Name the blood parasite species.
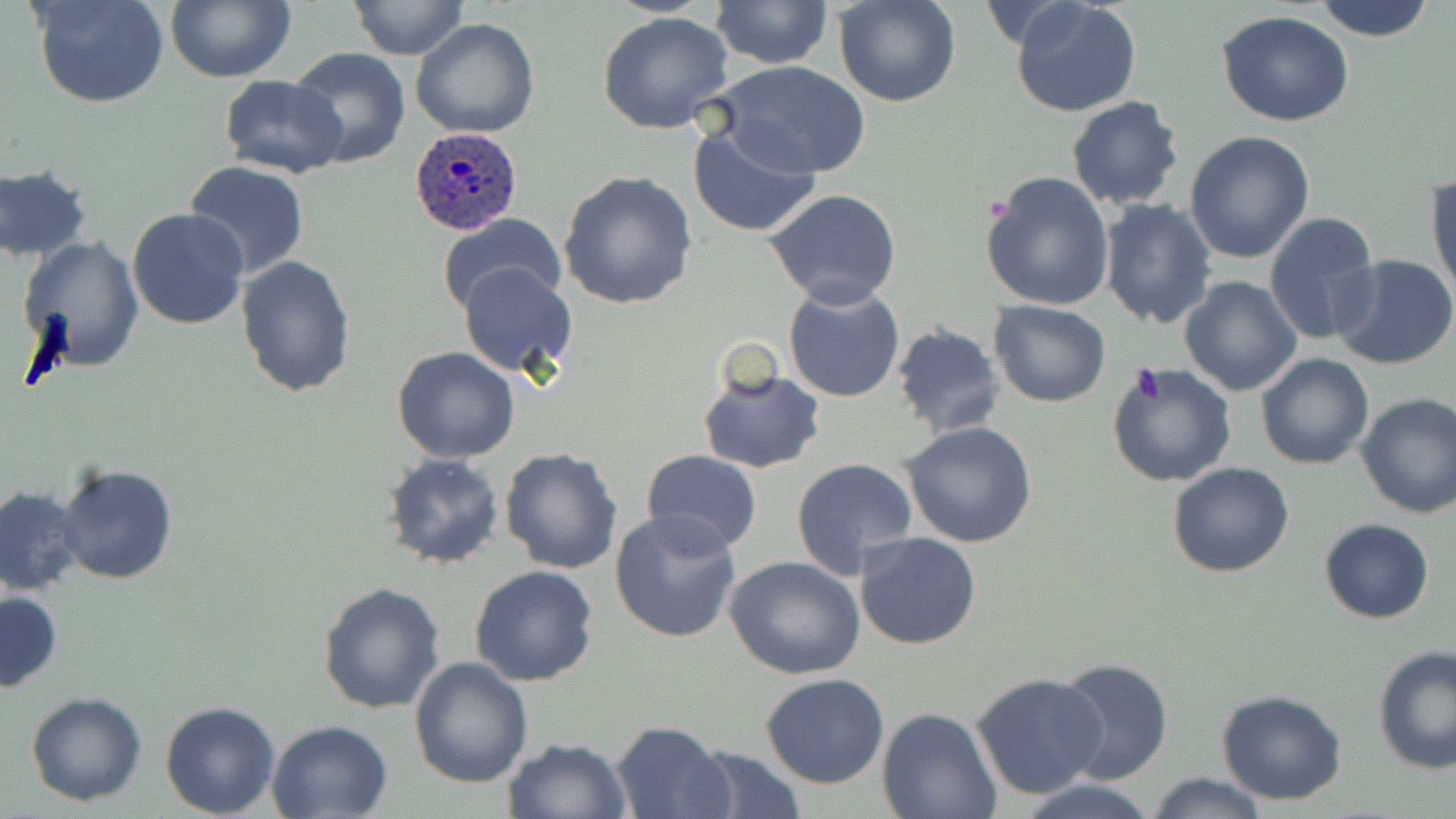
Plasmodium ovale.

stain = May-Grünwald-Giemsa
modality = light microscopy
preparation = thin blood film
image size = 1456×819 pixels
magnification = 1000x
Plasmodium ovale-infected red blood cell locations = approximate bounding boxes as (x1, y1, x2, y2) in pixels: (408, 127, 523, 236)
field of view = one of a larger specimen
platelet locations = approximate bounding boxes as (x1, y1, x2, y2) in pixels: (1127, 362, 1165, 409)
uninfected red blood cell locations = approximate bounding boxes as (x1, y1, x2, y2) in pixels: (30, 0, 169, 108), (166, 0, 294, 83), (349, 0, 469, 62), (711, 0, 833, 70), (834, 0, 961, 107), (1009, 0, 1143, 118), (1311, 0, 1439, 42), (1216, 11, 1357, 128), (597, 12, 735, 135), (410, 18, 541, 138), (287, 48, 413, 170), (711, 60, 872, 180), (217, 73, 346, 178), (1064, 95, 1185, 210), (685, 121, 823, 239), (1185, 131, 1315, 263), (185, 160, 310, 280), (0, 163, 92, 264), (1426, 169, 1455, 299), (979, 170, 1114, 311), (557, 171, 699, 309), (763, 189, 903, 310), (1098, 198, 1218, 330), (126, 207, 249, 329), (1264, 211, 1381, 344), (435, 214, 568, 317), (19, 237, 142, 374), (1330, 253, 1456, 371), (237, 256, 356, 398), (458, 263, 577, 376), (1178, 275, 1302, 398), (782, 283, 906, 403), (988, 299, 1110, 407), (892, 323, 1005, 440), (392, 346, 522, 463), (1255, 354, 1374, 471), (1106, 363, 1238, 486), (696, 366, 824, 474), (1355, 392, 1456, 520), (900, 421, 1037, 548), (499, 448, 622, 574), (641, 451, 764, 554), (381, 452, 507, 571), (791, 458, 918, 579), (56, 462, 180, 585), (1167, 462, 1295, 579), (0, 486, 90, 597), (610, 509, 743, 645), (1318, 518, 1435, 624), (855, 531, 983, 650), (724, 557, 866, 679), (470, 564, 598, 686), (317, 581, 446, 715), (1, 589, 63, 693), (1371, 646, 1456, 773), (408, 656, 532, 789), (1052, 657, 1174, 784), (971, 671, 1109, 799), (760, 674, 889, 790), (1215, 688, 1349, 806), (26, 690, 146, 806), (160, 700, 280, 818), (876, 709, 1002, 819), (266, 719, 395, 819), (609, 720, 733, 818), (501, 736, 631, 819), (688, 744, 806, 818), (1147, 774, 1271, 818), (1013, 777, 1160, 818)